Assess this cell for malaria.
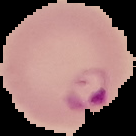
Parasitized.

preparation = thin blood film
image size = 136×136 pixels
image type = cell region segmented out of the field of view; surrounding area masked to black